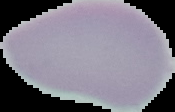
Summary:
  - Image size: 175×112 pixels
  - Image type: segmented cell region with the area outside set to black
  - Preparation: thin blood film
  - Result: no malaria parasites detected